Comment on the morphology of the red blood cells.
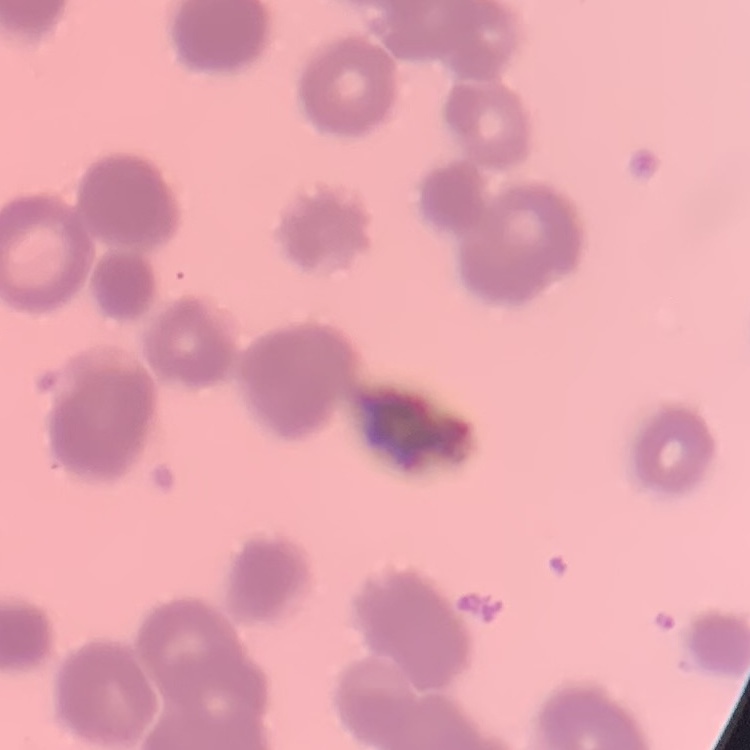

They show rouleaux formation.

Thin blood smear. Stained with either Field's or Giemsa. Square crop of a larger photomicrograph.